Locate every blood parasite and identify its species.
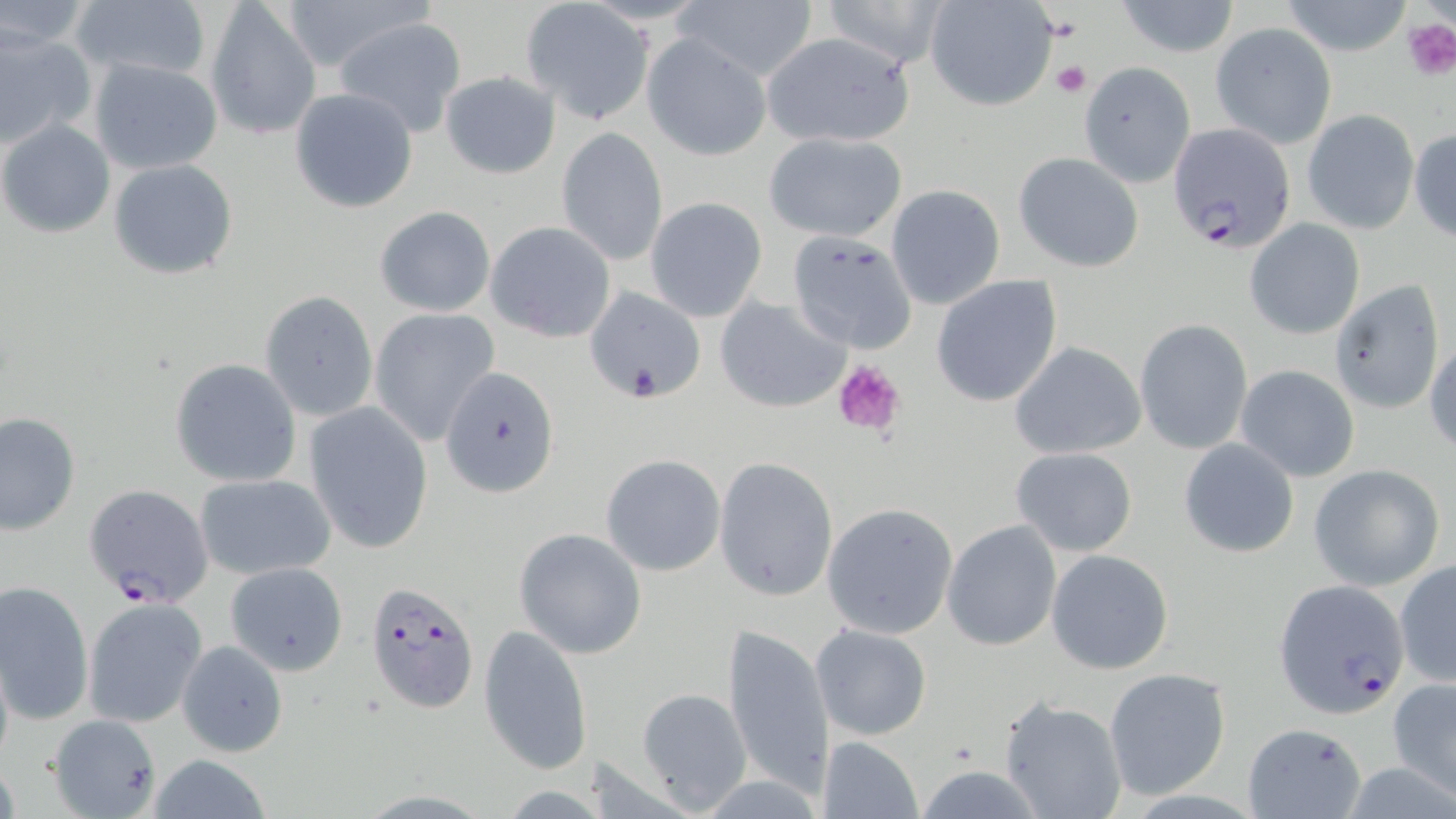

Approximate bounding boxes as (x1, y1, x2, y2) in pixels.
Plasmodium falciparum-infected red blood cells: (1169, 126, 1295, 252), (366, 579, 479, 713), (1274, 579, 1411, 720).
No Plasmodium ovale, Plasmodium malariae, Plasmodium vivax, Babesia divergens, or Trypanosoma brucei observed.

Uninfected red blood cell locations: (68, 0, 212, 86), (272, 0, 434, 76), (923, 0, 1058, 112), (1113, 0, 1243, 58), (0, 1, 96, 53), (819, 1, 952, 68), (1279, 1, 1414, 56), (205, 2, 322, 139), (521, 2, 652, 124), (671, 2, 820, 84), (334, 15, 467, 137), (1211, 20, 1337, 150), (0, 24, 94, 151), (759, 31, 917, 150), (643, 34, 773, 162), (88, 57, 225, 174), (1078, 62, 1196, 188), (439, 70, 561, 179), (288, 88, 419, 213), (1303, 109, 1418, 234), (0, 119, 115, 237), (1409, 125, 1456, 241), (556, 128, 669, 266), (762, 128, 908, 242), (1013, 152, 1144, 273), (108, 158, 239, 280), (885, 184, 1006, 310), (645, 198, 767, 322), (373, 205, 496, 318), (486, 220, 617, 343), (1245, 220, 1365, 340), (787, 231, 917, 355), (931, 274, 1063, 407), (1329, 279, 1445, 416), (585, 285, 708, 406), (258, 289, 378, 424), (717, 297, 852, 414), (366, 308, 501, 445), (1134, 319, 1253, 454), (1426, 339, 1456, 455), (1011, 343, 1147, 459), (170, 358, 300, 487), (440, 364, 560, 498), (1235, 364, 1360, 482), (304, 401, 434, 553), (0, 410, 80, 535), (1178, 438, 1299, 559), (1011, 447, 1137, 557), (600, 454, 727, 575), (714, 456, 838, 601), (1307, 465, 1444, 590), (194, 473, 336, 580), (84, 483, 213, 608), (822, 502, 958, 638), (942, 519, 1063, 651), (513, 527, 648, 658), (1047, 549, 1174, 675), (1394, 559, 1456, 687), (223, 560, 350, 676), (0, 580, 93, 729), (82, 596, 207, 729), (722, 623, 832, 801), (480, 624, 593, 776), (810, 624, 932, 741), (178, 639, 288, 757), (1102, 667, 1231, 800), (1388, 678, 1456, 801), (633, 687, 753, 813), (998, 697, 1128, 819), (46, 716, 161, 815), (1242, 721, 1366, 818), (817, 736, 923, 818), (138, 755, 280, 818), (913, 765, 1047, 817). Platelet locations: (1401, 16, 1456, 78), (1050, 59, 1091, 98), (831, 359, 907, 437). Slide-level diagnosis: Plasmodium falciparum. Light microscopy. Image is 1456×819 pixels. 1000x magnification. One field of a larger specimen. Thin blood smear. May-Grünwald-Giemsa-stained preparation.